Point out each Plasmodium parasite.
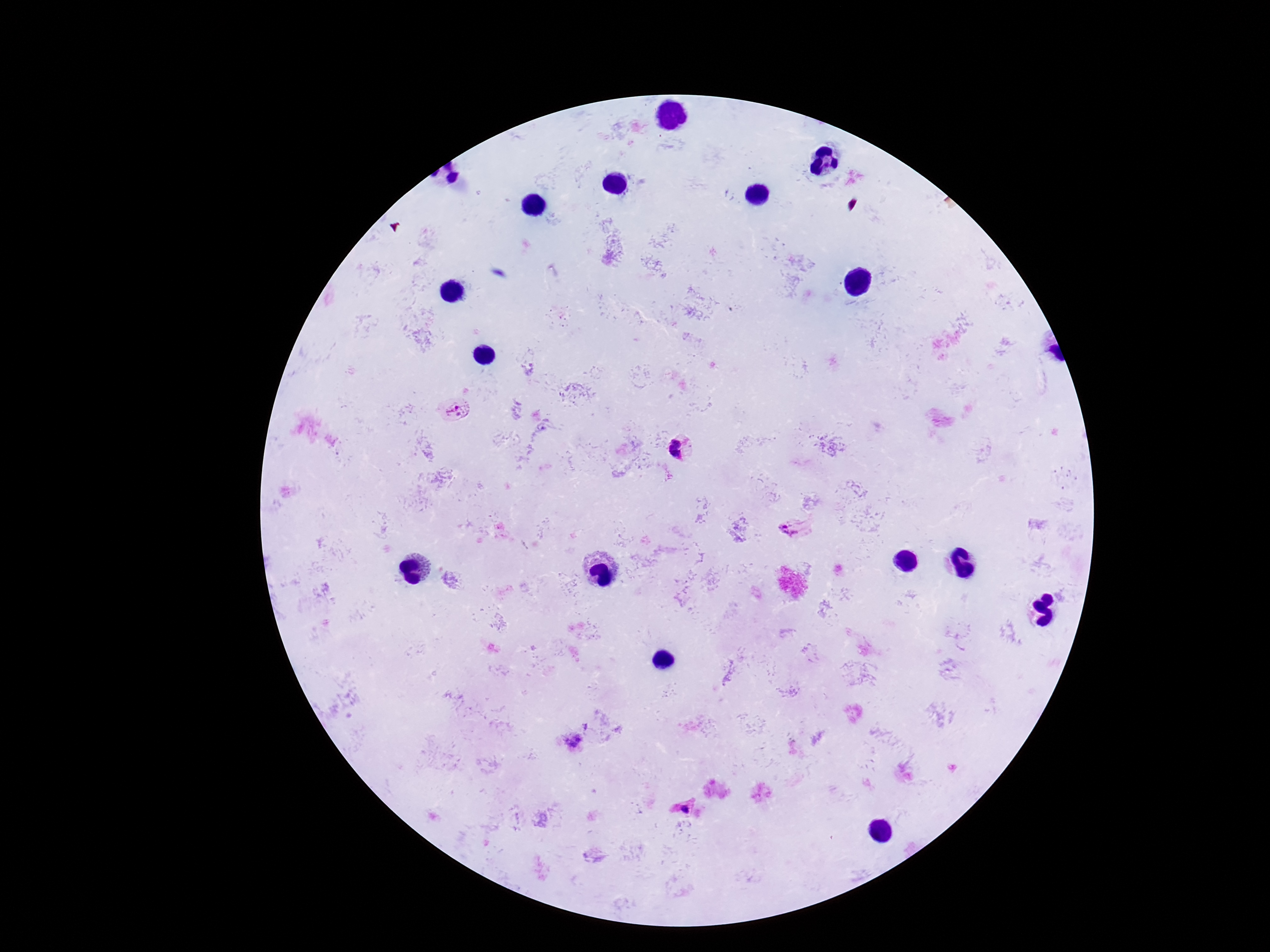

Approximate centers as [x, y] in pixels.
Plasmodium parasites: [454, 409], [682, 448], [793, 530], [573, 743], [684, 807].

Summary:
  - Capture: smartphone camera through the microscope eyepiece
  - Image size: 1270×952 pixels
  - Patient malaria status: infected
  - Magnification: 100x
  - Field of view: single
  - Preparation: thick blood smear
  - Stain: Giemsa